Describe the morphology of the erythrocytes.
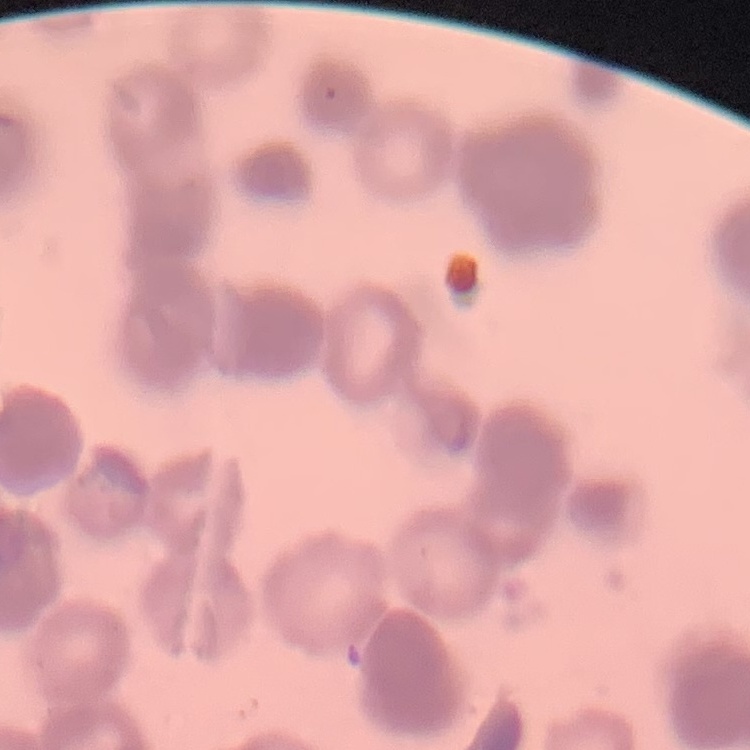
Rouleaux formation.

preparation = thin blood film
stain = Field's or Giemsa
image type = square crop of a larger photomicrograph